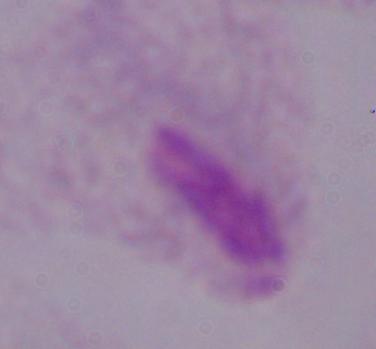

A trichomonad is shown. Photomicrograph. Captured at 1000x magnification.